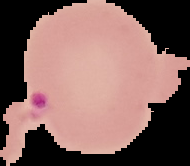

preparation: thin blood film
image_type: cell region segmented out of the field of view; surrounding area masked to black
result: malaria parasites detected
image_size: 190×166 pixels